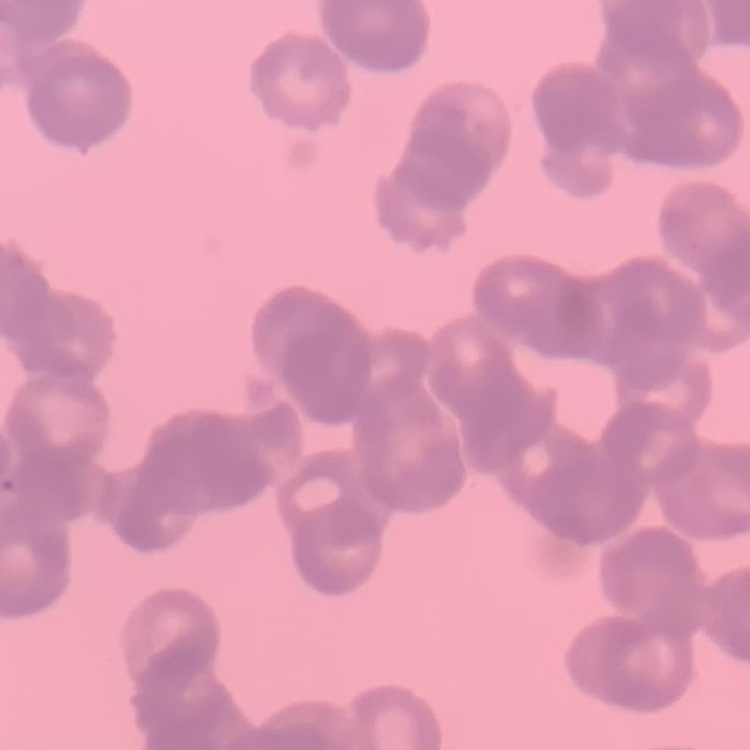
Summary:
  - Red blood cell morphology: rouleaux formation
  - Image type: one tile cut from a larger photomicrograph
  - Stain: Field's or Giemsa
  - Preparation: thin blood smear